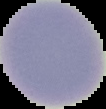
malaria status = uninfected
preparation = thin blood film
image type = cell region segmented out of the field of view; surrounding area masked to black
image size = 106×109 pixels